Give the position of every Plasmodium parasite.
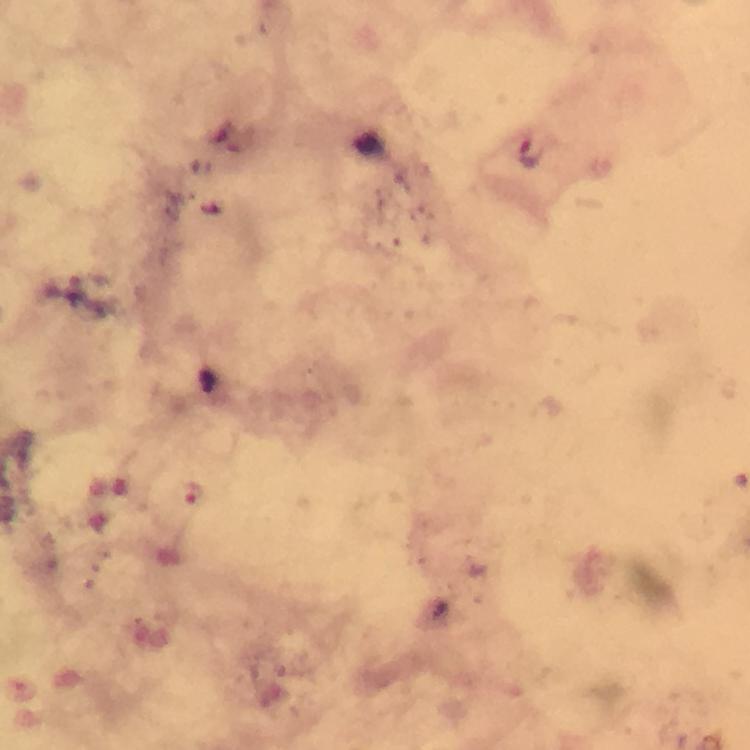

Approximate centers as [x, y] in pixels.
Plasmodium parasites: [531, 154], [193, 490].

{
  "image_size": "750×750 pixels",
  "preparation": "thick blood smear",
  "stain": "Giemsa",
  "magnification": "100x",
  "capture": "smartphone photograph through a microscope",
  "immersion_oil": "applied",
  "context": "from a diagnostic examination for malaria",
  "cropped_from": "a single field of view"
}